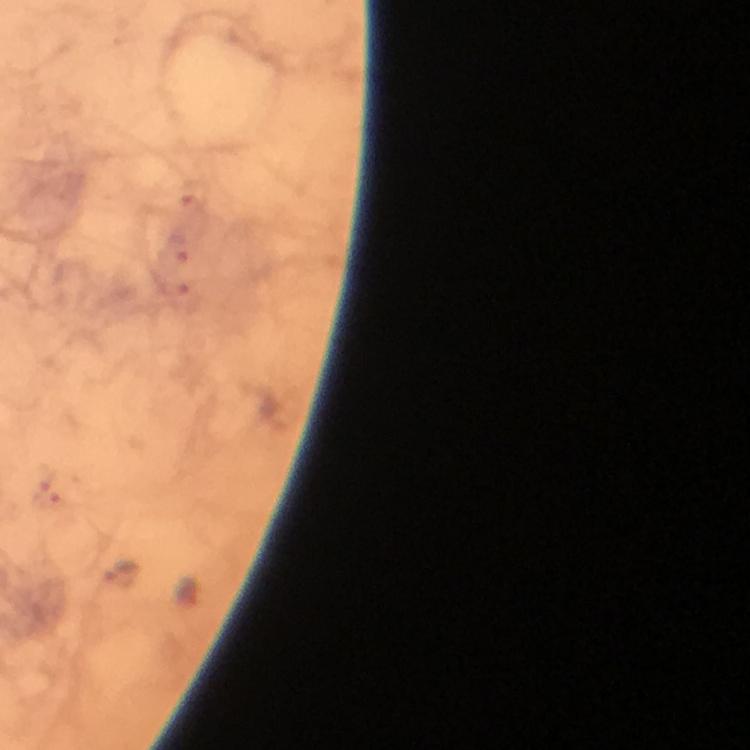
preparation = thick smear
immersion oil = used
magnification = 100x
cropped from = a single field of view
capture = smartphone camera through the microscope
malaria parasite locations = approximate centers as {x, y} in pixels: {193, 194}, {175, 249}, {179, 297}, {48, 494}
image size = 750×750 pixels
stain = Giemsa
context = from a malaria diagnostic workup